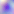
{
  "modality": "photomicrograph",
  "magnification": "400x",
  "identification": "Toxoplasma gondii"
}